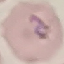
Summary:
  - Result: malaria parasites identified
  - Image type: cell patch, automatically extracted from a larger field of view and resized to 64 × 64 pixels
  - Preparation: thin blood film
  - Capture: smartphone through the microscope eyepiece
  - Stain: Giemsa